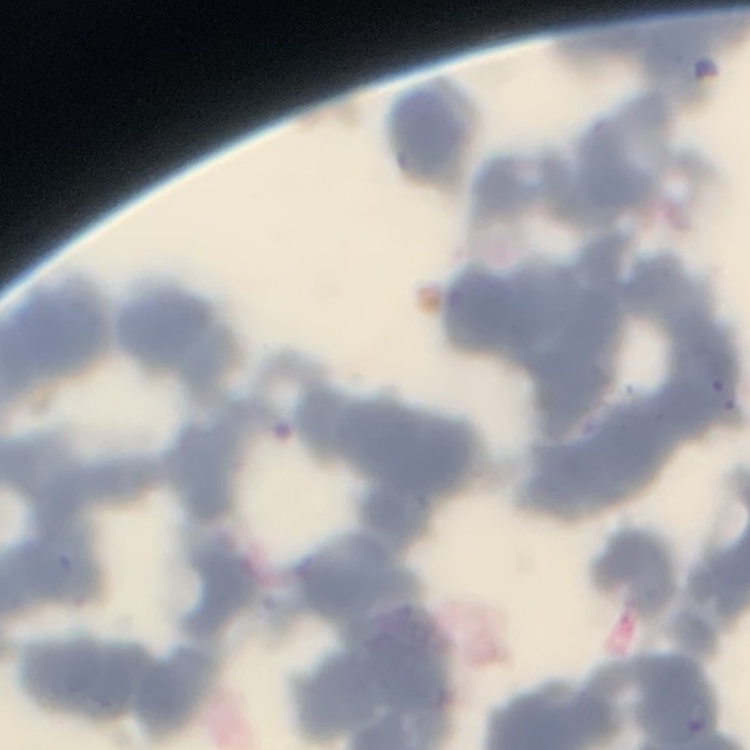

Summary:
  - Erythrocyte morphology: rouleaux formation
  - Stain: Field's or Giemsa
  - Image type: square crop of a larger photomicrograph
  - Preparation: thin blood smear